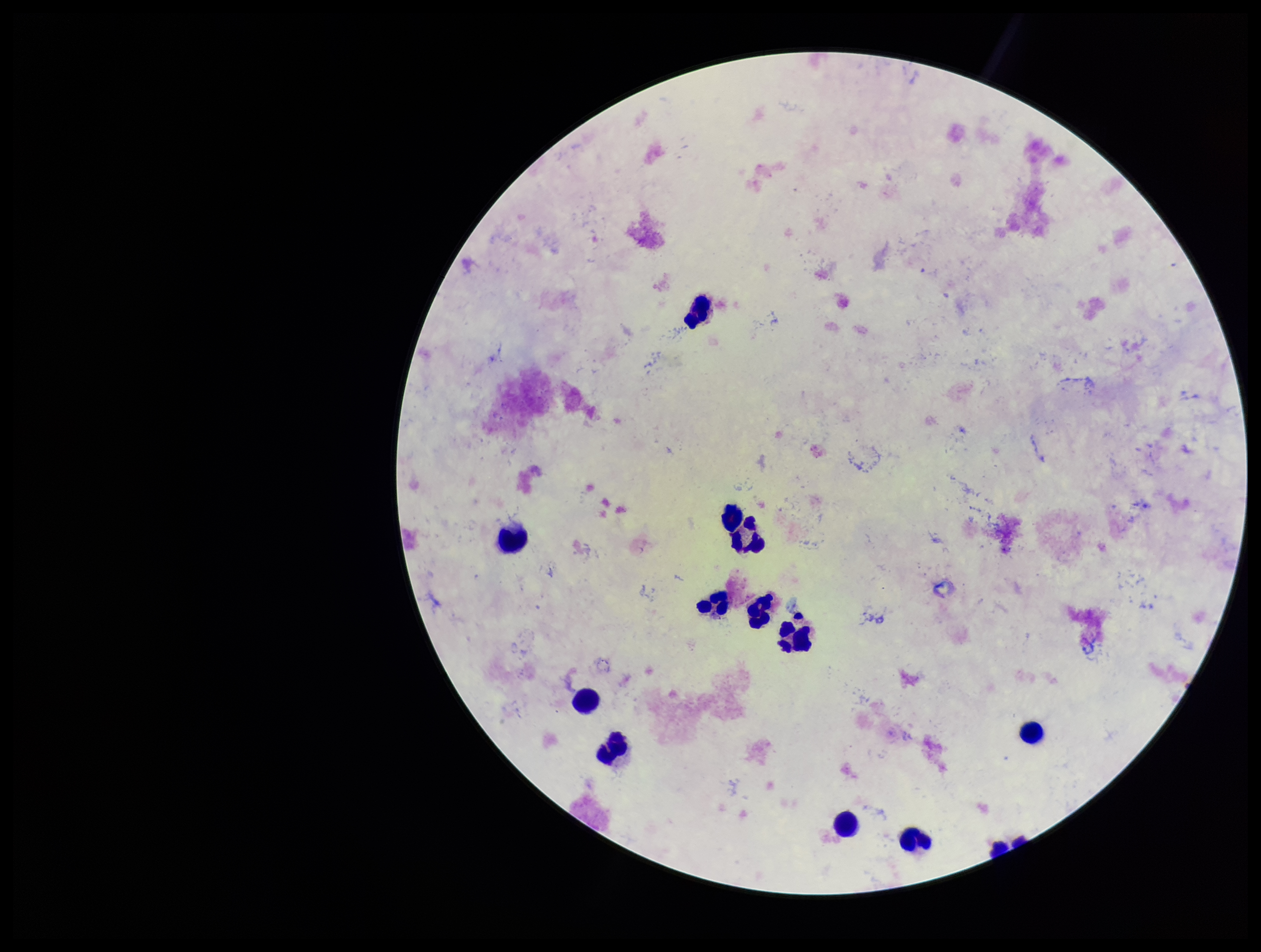
Patient malaria status: infected. Parasite count: 0. Preparation: thick smear. Image is 1261×952 pixels. Species reported for this patient: Plasmodium vivax. Leukocyte count: 12. One field from this slide. Plasmodium parasites: none identified. Giemsa stain. Photographed through the microscope eyepiece with a smartphone camera.